Classify this cell by malaria status.
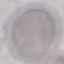

It is uninfected.

Automatically extracted cell patch, resized to 64 × 64 pixels. Thin blood smear. Giemsa-stained preparation. Photographed with a smartphone camera at the microscope eyepiece.